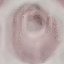 Result: negative for malaria parasites. Giemsa-stained preparation. Automatically extracted cell patch, resized to 64 × 64 pixels. Thin blood smear. Photographed with a smartphone camera at the microscope eyepiece.